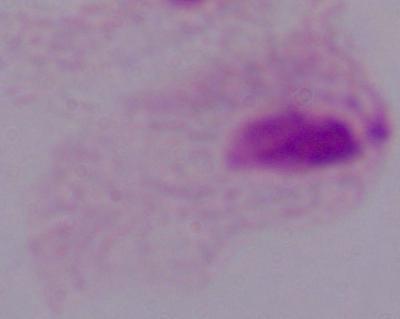 Photomicrograph. 1000x magnification. A trichomonad is seen.